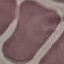

malaria status = uninfected
stain = Giemsa
preparation = thin blood smear
image type = automatically extracted cell patch, resized to 64 × 64 pixels
capture = smartphone through the microscope eyepiece